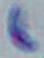
Photomicrograph. Toxoplasma gondii is shown. 1000x magnification.